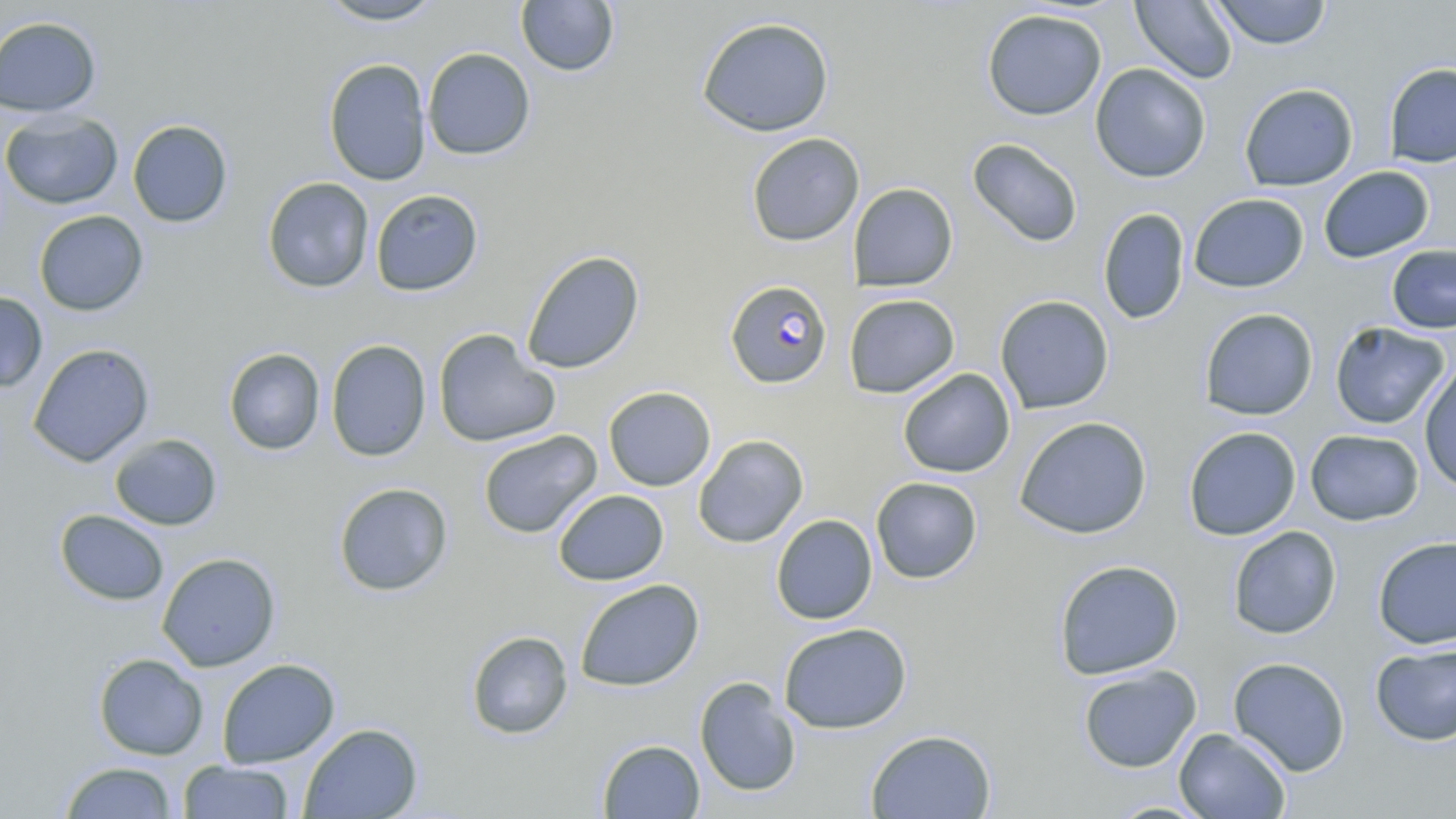
slide-level diagnosis = Plasmodium falciparum
stain = May-Grünwald-Giemsa
modality = optical microscopy
image size = 1456×819 pixels
field of view = one of a larger specimen
magnification = 1000x
preparation = thin blood smear
uninfected red blood cell locations = approximate bounding boxes as (x1, y1, x2, y2) in pixels: (317, 0, 446, 26), (515, 0, 620, 77), (1130, 0, 1238, 84), (1208, 0, 1333, 49), (981, 8, 1107, 121), (0, 15, 102, 117), (696, 16, 834, 137), (422, 47, 536, 160), (322, 58, 431, 186), (1383, 62, 1456, 168), (1089, 63, 1212, 183), (1239, 83, 1359, 191), (0, 111, 123, 209), (128, 119, 233, 227), (746, 132, 865, 246), (967, 138, 1083, 248), (1318, 165, 1435, 263), (262, 176, 374, 293), (848, 182, 958, 291), (370, 189, 484, 296), (1189, 193, 1309, 292), (1097, 208, 1190, 325), (33, 210, 148, 316), (1387, 244, 1456, 333), (521, 250, 645, 374), (0, 291, 48, 393), (843, 293, 960, 398), (995, 294, 1115, 414), (1199, 307, 1319, 420), (1329, 321, 1451, 430), (433, 328, 559, 448), (326, 339, 430, 462), (27, 343, 155, 467), (223, 347, 325, 455), (1419, 363, 1456, 492), (898, 368, 1016, 478), (603, 386, 716, 491), (1014, 415, 1152, 539), (1183, 426, 1301, 540), (1305, 429, 1424, 526), (477, 430, 603, 539), (109, 433, 223, 531), (693, 434, 809, 548), (870, 476, 983, 584), (334, 482, 453, 596), (553, 489, 669, 586), (54, 509, 169, 606), (771, 514, 877, 624), (1228, 525, 1342, 639), (1373, 535, 1456, 649), (157, 552, 280, 671), (1053, 559, 1184, 679), (575, 579, 704, 691), (778, 622, 912, 734), (466, 630, 573, 739), (1370, 642, 1456, 746), (93, 653, 208, 760), (1227, 656, 1351, 777), (216, 658, 340, 768), (1077, 664, 1202, 773), (694, 676, 802, 798), (299, 723, 423, 818), (1173, 727, 1291, 818), (865, 728, 997, 819), (598, 739, 705, 818), (178, 760, 294, 818), (58, 761, 179, 818), (1104, 800, 1217, 818)
Plasmodium falciparum-infected red blood cell locations = approximate bounding boxes as (x1, y1, x2, y2) in pixels: (724, 280, 833, 388)